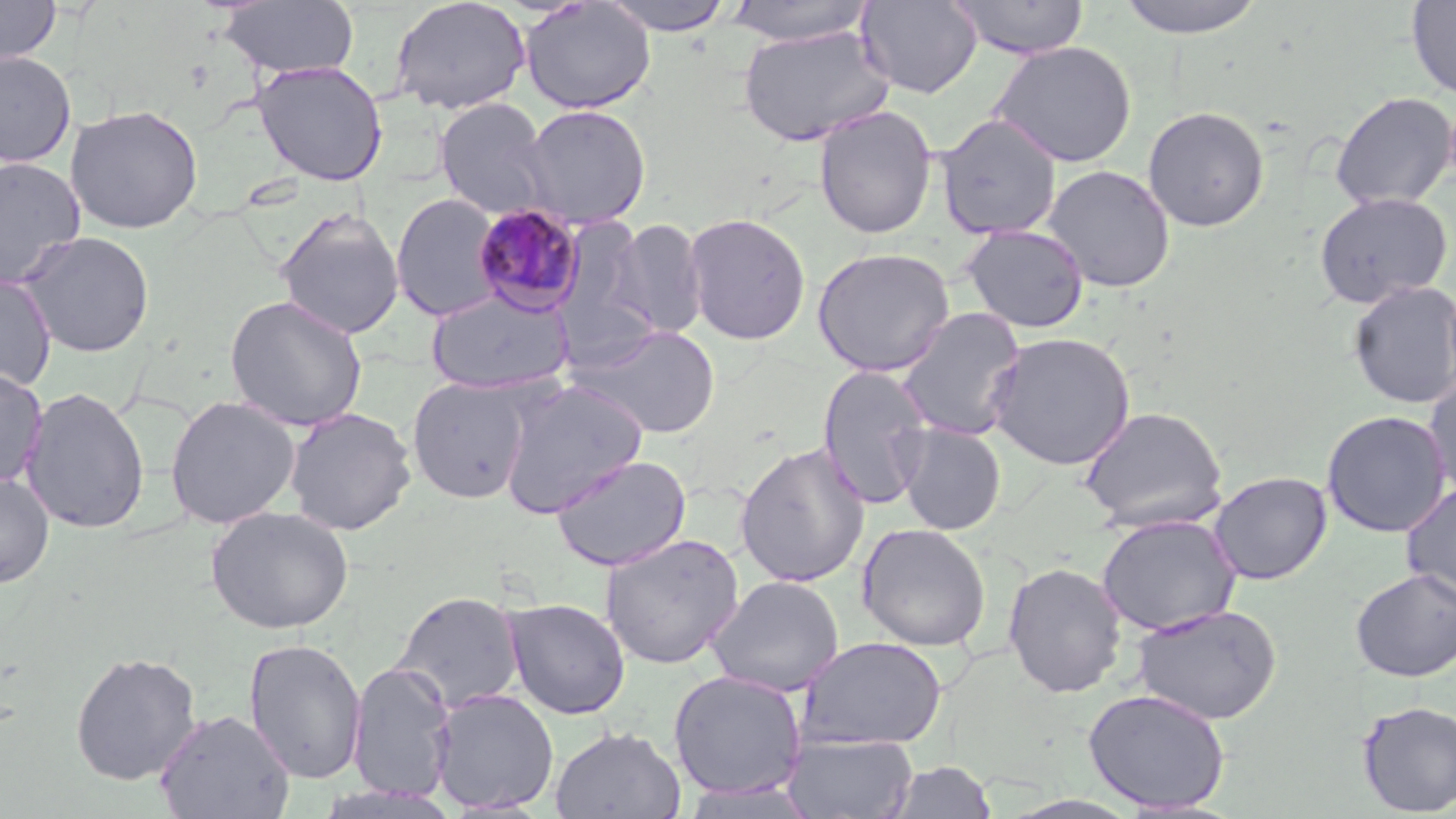 Approximate bounding boxes as (x1,y1)-(x2,y2) corner pairs in pixels. Plasmodium malariae-infected red blood cell locations: (472,202)-(587,317). Uninfected red blood cell locations: (0,0)-(62,66), (389,0)-(531,115), (599,0)-(737,36), (857,0)-(982,99), (950,0)-(1090,60), (1112,0)-(1269,39), (1406,0)-(1456,100), (219,1)-(360,80), (722,1)-(876,46), (520,2)-(656,114), (737,24)-(894,147), (989,41)-(1137,169), (0,50)-(76,167), (252,61)-(388,186), (1330,91)-(1456,211), (434,98)-(555,221), (66,103)-(204,234), (520,105)-(651,229), (813,105)-(938,240), (1142,106)-(1270,232), (935,113)-(1062,240), (0,156)-(86,289), (1042,164)-(1176,292), (1313,192)-(1453,308), (391,193)-(505,322), (275,208)-(405,340), (683,212)-(812,345), (607,218)-(709,339), (959,224)-(1090,333), (17,230)-(156,358), (812,247)-(956,376), (0,272)-(57,394), (1347,279)-(1456,410), (427,289)-(574,394), (224,294)-(368,432), (895,307)-(1028,441), (575,323)-(722,438), (986,332)-(1136,470), (817,364)-(935,510), (0,367)-(48,490), (1423,372)-(1456,500), (407,376)-(535,504), (497,379)-(649,518), (20,386)-(150,535), (165,395)-(300,529), (1079,405)-(1228,532), (283,406)-(417,535), (1321,409)-(1452,538), (896,423)-(1006,535), (734,441)-(871,588), (551,454)-(692,572), (1207,471)-(1332,585), (0,473)-(55,588), (1400,481)-(1456,608), (206,505)-(354,635), (1096,514)-(1242,636), (856,523)-(991,651), (600,532)-(744,669), (1002,561)-(1128,698), (1350,567)-(1456,682), (708,575)-(844,697), (392,590)-(525,713), (502,598)-(630,719), (1131,603)-(1282,725), (797,635)-(948,750), (243,637)-(367,785), (70,650)-(202,786), (347,660)-(456,803), (668,670)-(807,800), (429,687)-(560,814), (1083,687)-(1231,813), (1356,700)-(1456,816), (154,708)-(295,819), (550,726)-(685,818), (783,733)-(918,818), (884,760)-(997,818). Slide-level diagnosis: Plasmodium malariae. May-Grünwald-Giemsa-stained preparation. Thin blood smear. Single field of view. Light microscopy. Captured at 1000x magnification. Image is 1456×819 pixels.